State which parasite is depicted.
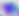
This is Toxoplasma gondii.

400x magnification. Micrograph.